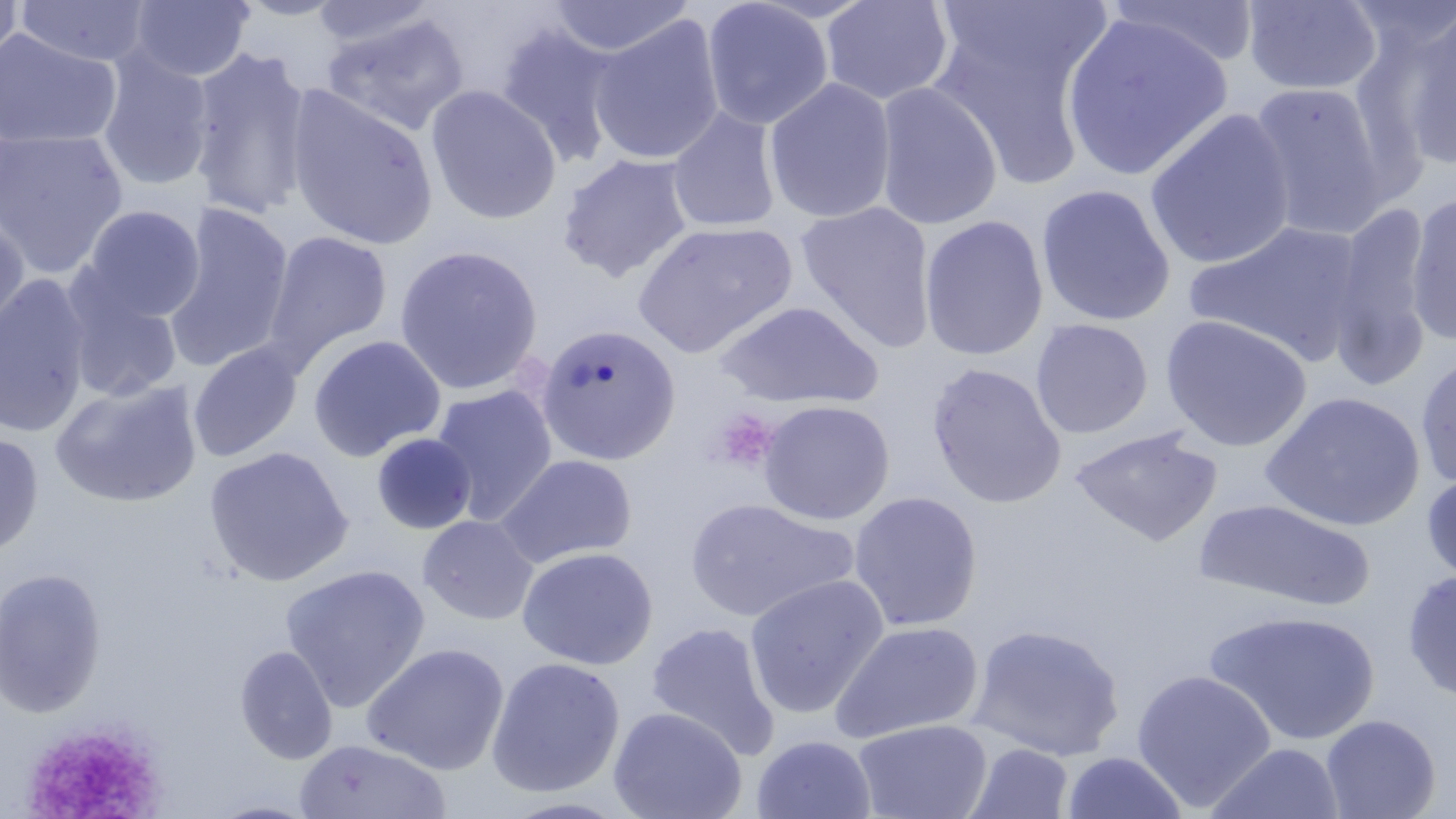
Approximate bounding boxes as named x1/y1/x2/y2 corners in pixels. Uninfected red blood cell locations: (x1=0, y1=0, x2=23, y2=73), (x1=128, y1=0, x2=255, y2=82), (x1=235, y1=0, x2=351, y2=20), (x1=701, y1=0, x2=834, y2=130), (x1=819, y1=0, x2=954, y2=106), (x1=16, y1=1, x2=153, y2=68), (x1=309, y1=1, x2=438, y2=49), (x1=547, y1=1, x2=696, y2=58), (x1=1104, y1=1, x2=1262, y2=67), (x1=1242, y1=1, x2=1383, y2=96), (x1=926, y1=6, x2=1106, y2=190), (x1=1395, y1=8, x2=1456, y2=173), (x1=1060, y1=12, x2=1234, y2=182), (x1=320, y1=13, x2=469, y2=138), (x1=588, y1=13, x2=725, y2=166), (x1=494, y1=21, x2=625, y2=170), (x1=0, y1=28, x2=122, y2=150), (x1=187, y1=45, x2=315, y2=222), (x1=96, y1=48, x2=215, y2=192), (x1=764, y1=78, x2=897, y2=224), (x1=873, y1=82, x2=1003, y2=231), (x1=1247, y1=82, x2=1393, y2=241), (x1=283, y1=85, x2=438, y2=251), (x1=425, y1=85, x2=563, y2=225), (x1=667, y1=106, x2=782, y2=234), (x1=1144, y1=108, x2=1298, y2=270), (x1=0, y1=128, x2=128, y2=279), (x1=558, y1=153, x2=695, y2=283), (x1=8, y1=169, x2=197, y2=304), (x1=1035, y1=184, x2=1176, y2=327), (x1=1405, y1=192, x2=1456, y2=345), (x1=1327, y1=200, x2=1435, y2=389), (x1=795, y1=201, x2=938, y2=353), (x1=162, y1=203, x2=295, y2=371), (x1=79, y1=205, x2=207, y2=323), (x1=0, y1=210, x2=30, y2=343), (x1=919, y1=214, x2=1049, y2=361), (x1=1186, y1=219, x2=1367, y2=365), (x1=631, y1=220, x2=798, y2=358), (x1=261, y1=229, x2=393, y2=371), (x1=394, y1=245, x2=543, y2=395), (x1=0, y1=275, x2=94, y2=438), (x1=63, y1=280, x2=184, y2=402), (x1=714, y1=300, x2=884, y2=410), (x1=1160, y1=314, x2=1312, y2=452), (x1=1030, y1=318, x2=1153, y2=439), (x1=535, y1=324, x2=681, y2=466), (x1=307, y1=334, x2=446, y2=461), (x1=188, y1=342, x2=303, y2=463), (x1=1414, y1=352, x2=1456, y2=489), (x1=927, y1=363, x2=1067, y2=508), (x1=50, y1=379, x2=203, y2=509), (x1=430, y1=385, x2=557, y2=523), (x1=1260, y1=390, x2=1425, y2=532), (x1=757, y1=400, x2=894, y2=525), (x1=1069, y1=426, x2=1222, y2=546), (x1=0, y1=431, x2=44, y2=559), (x1=372, y1=433, x2=476, y2=534), (x1=204, y1=446, x2=353, y2=586), (x1=496, y1=454, x2=636, y2=569), (x1=1421, y1=471, x2=1456, y2=585), (x1=848, y1=491, x2=983, y2=631), (x1=683, y1=498, x2=857, y2=623), (x1=1193, y1=499, x2=1376, y2=611), (x1=418, y1=514, x2=539, y2=625), (x1=517, y1=546, x2=658, y2=670), (x1=279, y1=564, x2=431, y2=711), (x1=0, y1=567, x2=107, y2=720), (x1=1402, y1=571, x2=1456, y2=704), (x1=743, y1=574, x2=890, y2=719), (x1=1205, y1=610, x2=1382, y2=747), (x1=829, y1=620, x2=984, y2=744), (x1=645, y1=621, x2=781, y2=760), (x1=967, y1=624, x2=1125, y2=761), (x1=360, y1=643, x2=510, y2=776), (x1=234, y1=644, x2=338, y2=765), (x1=486, y1=657, x2=625, y2=798), (x1=1131, y1=669, x2=1277, y2=812), (x1=607, y1=706, x2=747, y2=819), (x1=1321, y1=714, x2=1441, y2=819), (x1=852, y1=718, x2=993, y2=819), (x1=751, y1=734, x2=877, y2=819), (x1=294, y1=738, x2=451, y2=819), (x1=964, y1=742, x2=1074, y2=818), (x1=1206, y1=742, x2=1346, y2=819), (x1=1061, y1=750, x2=1188, y2=819), (x1=501, y1=798, x2=634, y2=818), (x1=204, y1=799, x2=324, y2=819). Platelet locations: (x1=709, y1=408, x2=780, y2=475), (x1=21, y1=723, x2=163, y2=819). Slide-level diagnosis: negative for blood parasites. May-Grünwald-Giemsa-stained preparation. 1000x magnification. Optical microscopy. Image is 1456×819 pixels. Thin blood smear. One field of a larger specimen.